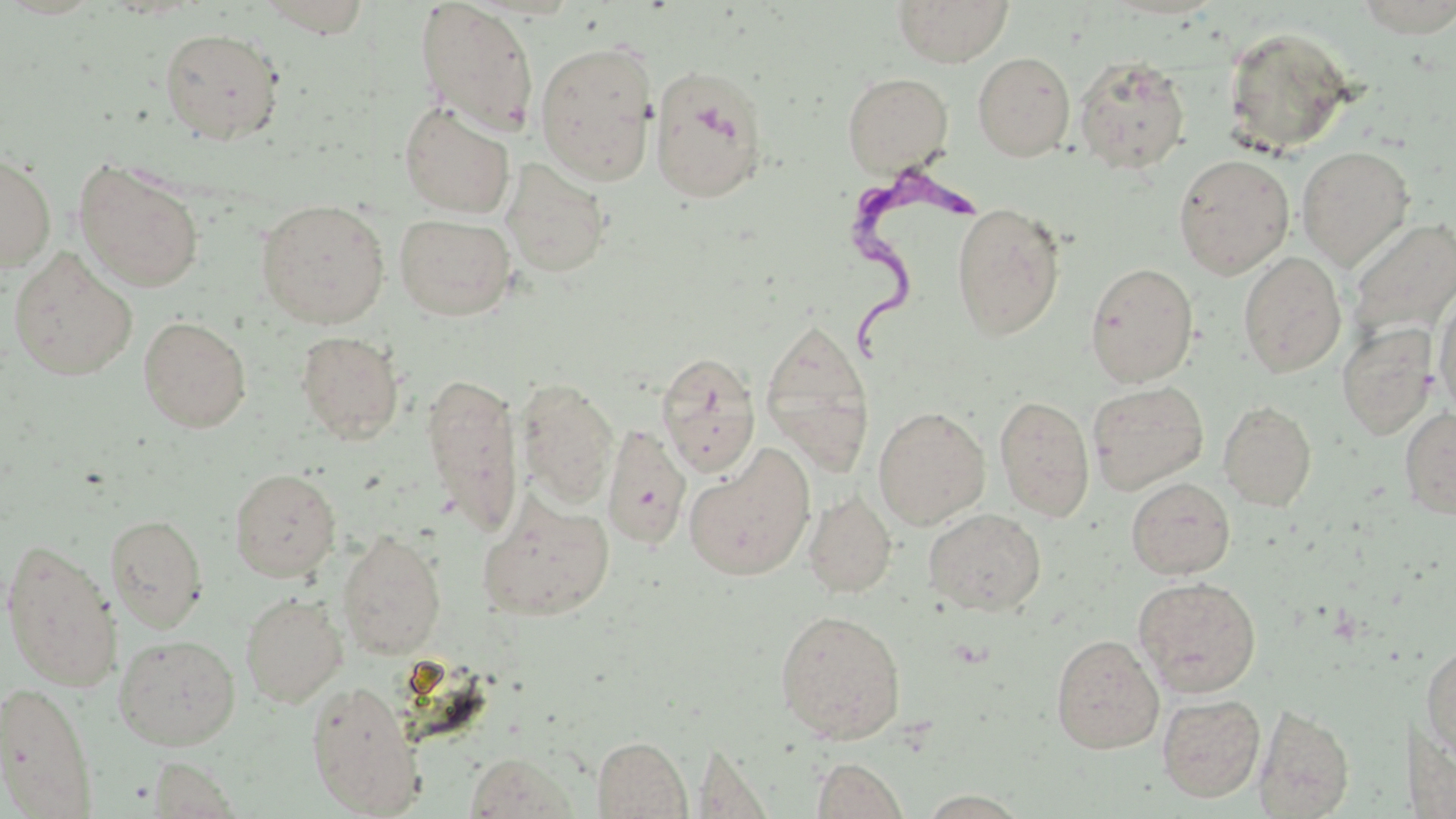
Summary:
  - Coordinate format: approximate bounding boxes as (x1,y1)-(x2,y2) corner pairs in pixels
  - Trypanosoma brucei locations: (849,163)-(991,376)
  - Uninfected red blood cell locations: (256,0)-(373,36), (415,0)-(540,134), (892,0)-(1015,67), (1351,0)-(1456,36), (1222,24)-(1358,156), (159,27)-(286,145), (533,40)-(659,185), (972,52)-(1076,161), (1074,55)-(1191,175), (648,64)-(771,203), (842,71)-(953,175), (399,100)-(515,218), (1296,145)-(1415,270), (0,153)-(57,272), (1172,153)-(1295,279), (502,158)-(612,279), (74,159)-(205,292), (256,199)-(390,328), (950,201)-(1066,340), (394,214)-(517,321), (1347,217)-(1456,345), (7,248)-(138,381), (1238,251)-(1347,377), (1084,262)-(1199,387), (1433,289)-(1456,420), (138,316)-(251,432), (759,317)-(875,476), (1337,323)-(1438,439), (295,330)-(405,444), (655,350)-(760,476), (421,372)-(525,536), (516,378)-(619,507), (1087,381)-(1208,495), (994,395)-(1095,522), (1218,400)-(1317,511), (873,406)-(990,530), (1399,407)-(1456,519), (602,424)-(691,550), (683,445)-(816,582), (229,468)-(341,581), (1126,477)-(1235,579), (803,491)-(896,598), (478,495)-(616,620), (923,508)-(1047,616), (105,513)-(208,632), (337,529)-(447,659), (1,538)-(121,689), (1132,576)-(1262,697), (240,592)-(348,706), (774,608)-(907,743), (113,633)-(241,750), (1050,634)-(1164,753), (1421,642)-(1456,761), (305,679)-(425,816), (1,680)-(98,818), (1157,693)-(1265,802), (1253,703)-(1355,818), (592,735)-(691,818), (463,752)-(582,819), (148,757)-(241,817), (810,758)-(909,818), (917,790)-(1031,818)
  - Slide-level diagnosis: Trypanosoma brucei
  - Image size: 1456×819 pixels
  - Stain: May-Grünwald-Giemsa
  - Modality: optical microscopy
  - Magnification: 1000x
  - Preparation: thin blood smear
  - Field of view: one of a larger specimen